Assess this cell for malaria.
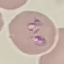

It is parasitized.

Thin smear of blood. Giemsa-stained preparation. Acquired by smartphone through the microscope eyepiece. Automatically extracted cell patch, resized to 64 × 64 pixels.